Classify this cell by malaria status.
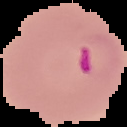

Parasitized.

Image is 127×127 pixels. From a thin blood smear. Cell region segmented out of the field of view; the surrounding area is masked to black.